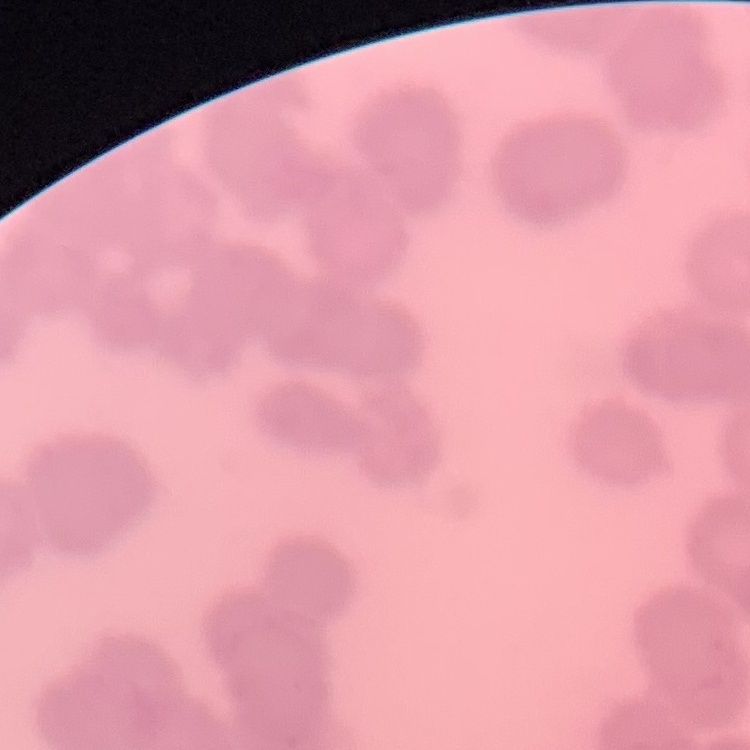

Summary:
  - Red blood cell morphology: rouleaux formation
  - Stain: Field's or Giemsa
  - Image type: one tile cut from a larger photomicrograph
  - Preparation: thin blood smear